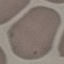
Result: negative for malaria parasites. Giemsa-stained preparation. Automatically extracted cell patch, resized to 64 × 64 pixels. Photographed with a smartphone camera at the microscope eyepiece. Thin smear of blood.